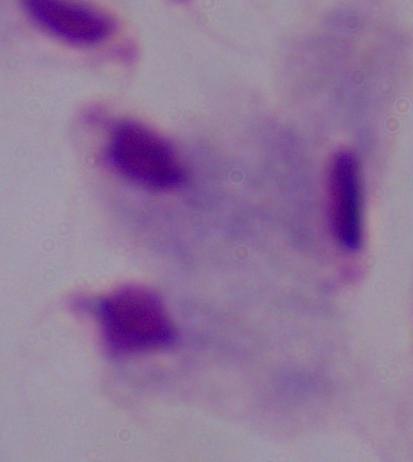
identification = trichomonad
magnification = 1000x
modality = micrograph